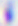
Summary:
  - Magnification: 400x
  - Identification: Toxoplasma gondii
  - Modality: micrograph